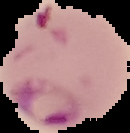

image_type: cell region segmented out of the field of view; surrounding area masked to black
malaria_status: parasitized
image_size: 130×133 pixels
preparation: thin blood film